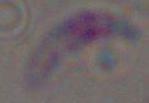
{
  "identification": "Toxoplasma gondii",
  "magnification": "1000x",
  "modality": "photomicrograph"
}